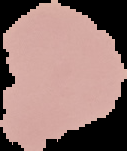
image size = 127×151 pixels
image type = segmented cell region on a black background
preparation = thin blood film
result = no Plasmodium parasites seen